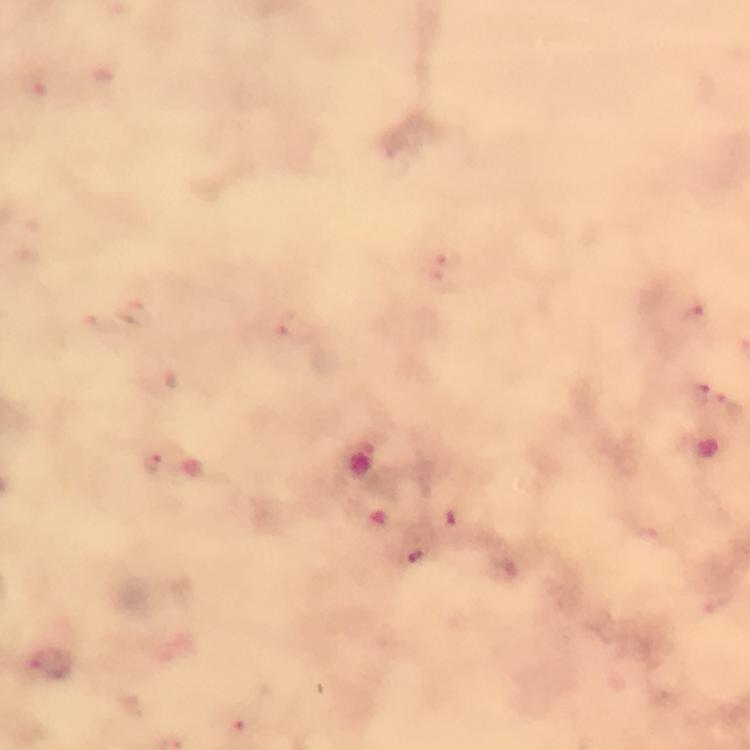
context: from a diagnostic examination for malaria
immersion_oil: applied
image_size: 750×750 pixels
malaria_parasite_locations: 'approximate centers as [x, y] in pixels: [448, 259], [697, 312], [294, 328], [700, 400], [730, 410], [155, 464], [416, 555], [52, 662]'
preparation: thick blood film
stain: Giemsa
cropped_from: a single field of view
magnification: 100x
capture: smartphone mounted on the microscope